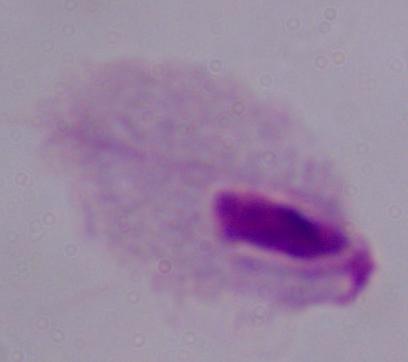

Summary:
  - Modality: micrograph
  - Identification: trichomonad
  - Magnification: 1000x